State which cell type is depicted.
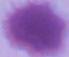
An erythrocyte.

{
  "magnification": "1000x",
  "modality": "photomicrograph"
}